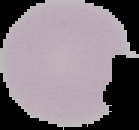
Summary:
  - Image type: cell region segmented out of the field of view; surrounding area masked to black
  - Preparation: thin blood smear
  - Result: no Plasmodium parasites detected
  - Image size: 139×130 pixels